State the preparation type.
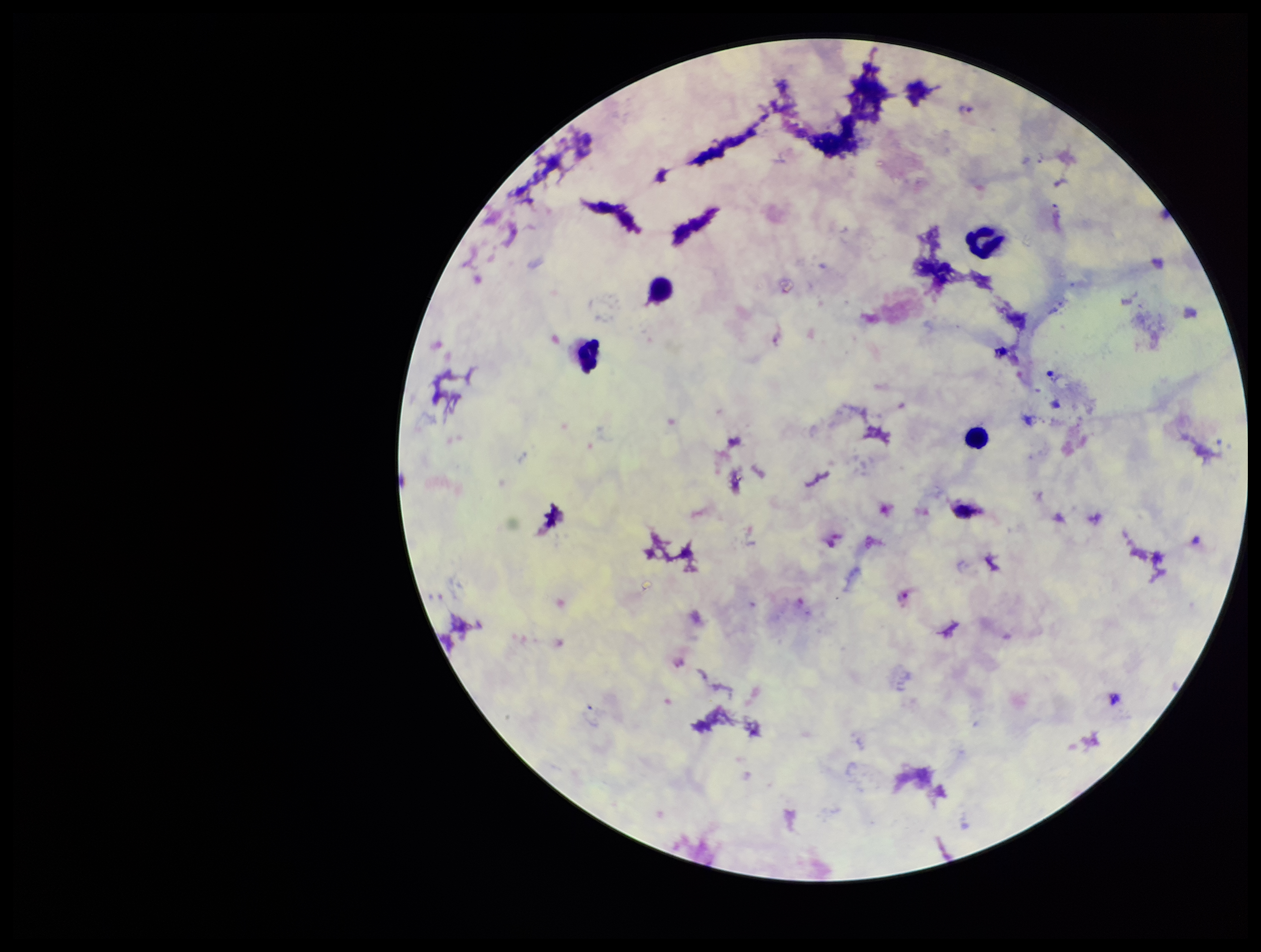

A thick smear.

Summary:
  - Image size: 1261×952 pixels
  - Leukocyte count: 4
  - Patient malaria status: infected
  - Species reported for this patient: Plasmodium vivax
  - Plasmodium parasites: seen
  - Stain: Giemsa
  - Parasite count: 5
  - Capture: smartphone photograph through the microscope eyepiece
  - Field of view: one from this slide